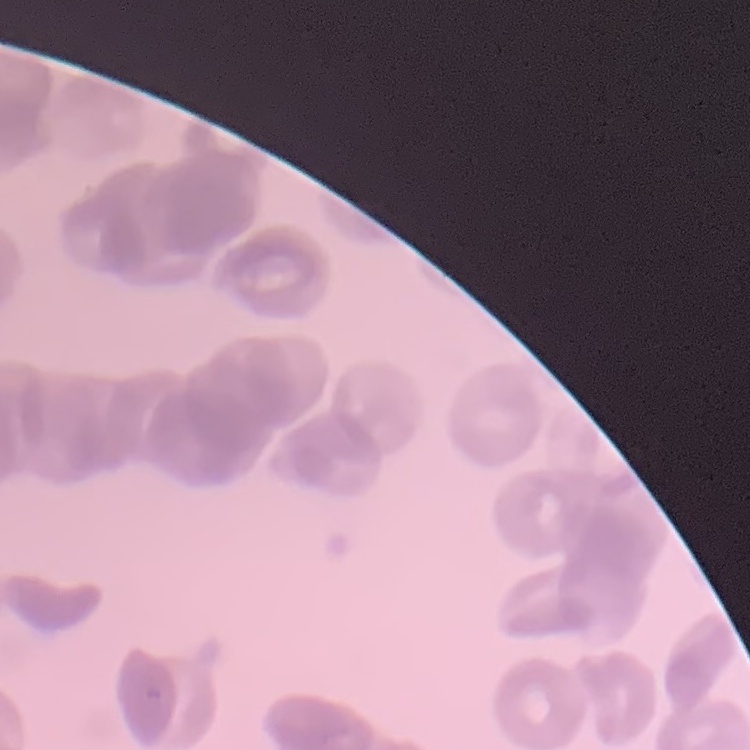
The erythrocytes exhibit rouleaux formation. Thin blood film. Stained with either Field's or Giemsa. One tile cut from a larger photomicrograph.